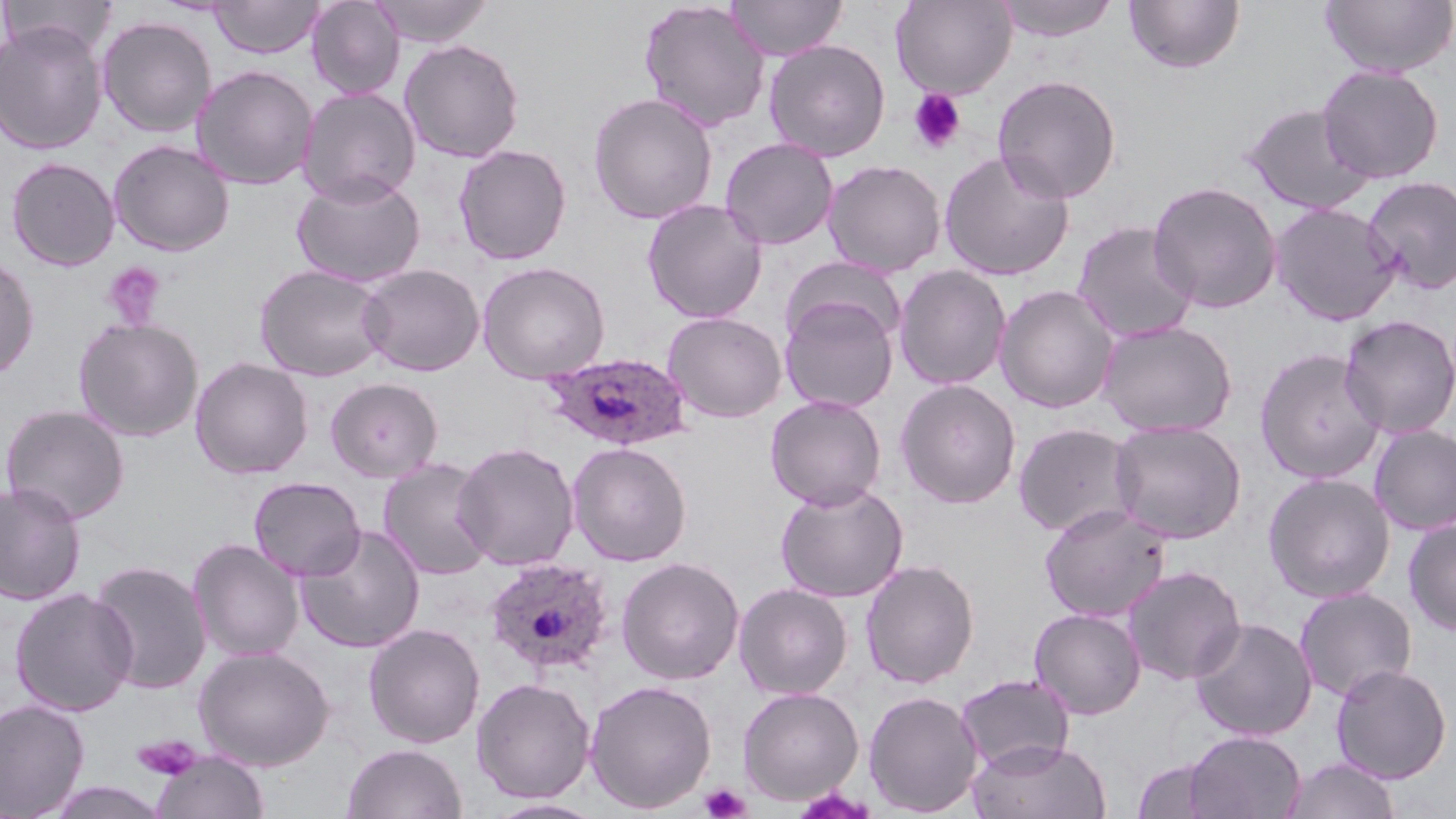

Approximate bounding boxes as (x1,y1)-(x2,y2) corner pairs in pixels. Platelet locations: (908,88)-(967,153), (101,262)-(166,331), (132,734)-(202,782), (700,783)-(752,819). Plasmodium ovale-infected red blood cell locations: (539,352)-(694,452), (482,557)-(615,676). Uninfected red blood cell locations: (1,0)-(117,59), (209,0)-(324,59), (306,0)-(405,100), (369,0)-(493,47), (638,0)-(771,133), (725,0)-(848,61), (890,0)-(1016,98), (995,0)-(1119,41), (1319,0)-(1456,77), (1123,1)-(1245,74), (97,15)-(217,138), (0,22)-(107,155), (399,39)-(525,163), (764,39)-(890,161), (1317,64)-(1445,183), (191,65)-(318,190), (992,74)-(1121,203), (297,87)-(422,206), (587,92)-(718,225), (1240,102)-(1377,216), (719,137)-(839,251), (108,139)-(235,256), (454,144)-(573,265), (939,151)-(1074,281), (6,157)-(120,271), (823,159)-(947,277), (292,172)-(426,288), (1361,176)-(1456,295), (1147,181)-(1283,314), (642,198)-(767,323), (1269,202)-(1401,326), (1071,221)-(1199,344), (0,254)-(40,381), (782,256)-(907,353), (476,260)-(611,383), (255,263)-(391,382), (358,263)-(484,376), (894,265)-(1012,391), (994,284)-(1120,413), (780,296)-(900,413), (663,311)-(787,423), (1338,314)-(1456,439), (74,317)-(204,442), (1097,319)-(1237,437), (1254,347)-(1386,484), (190,357)-(313,479), (325,377)-(443,482), (895,379)-(1021,509), (765,394)-(887,510), (1,404)-(130,524), (1109,420)-(1246,544), (1012,422)-(1139,538), (1369,424)-(1456,536), (567,441)-(692,566), (453,442)-(579,570), (378,458)-(496,579), (1263,472)-(1396,603), (248,476)-(365,581), (0,480)-(87,606), (774,481)-(909,602), (1039,503)-(1172,622), (1403,518)-(1456,635), (296,524)-(426,653), (187,538)-(305,662), (616,556)-(744,685), (860,559)-(979,688), (88,560)-(213,695), (1122,565)-(1246,685), (733,583)-(852,700), (9,587)-(138,717), (1294,587)-(1418,702), (1029,607)-(1146,719), (1188,617)-(1318,741), (363,623)-(486,748), (193,646)-(334,771), (1330,663)-(1452,784), (956,673)-(1075,775), (471,677)-(596,803), (584,679)-(717,813), (738,687)-(864,805), (863,690)-(983,817), (0,698)-(90,818), (1184,730)-(1306,819), (968,738)-(1111,819), (341,742)-(468,819), (150,750)-(270,818), (1281,756)-(1401,819), (1131,758)-(1219,818), (43,781)-(171,819), (484,798)-(607,818). Slide-level diagnosis: Plasmodium ovale. May-Grünwald-Giemsa stain. Light microscopy. One field of a larger specimen. Image is 1456×819 pixels. Thin blood smear. 1000x magnification.